Identify the preparation type.
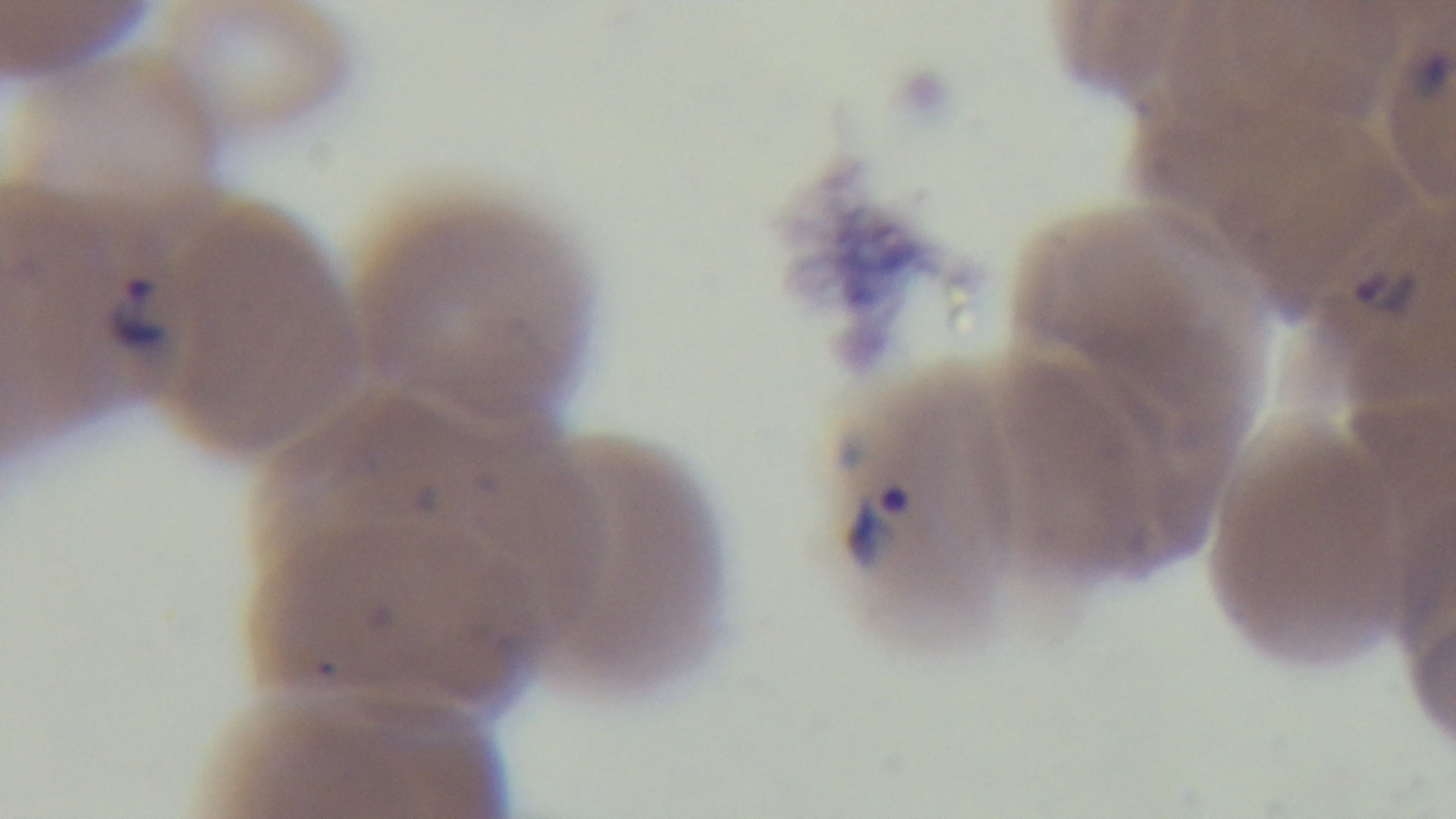

Thin.

100x oil-immersion objective. Photomicrograph. One field from the slide. Captured with a mounted 4K digital camera. Giemsa stain. Malaria status: infected.